Describe the morphology of the erythrocytes.
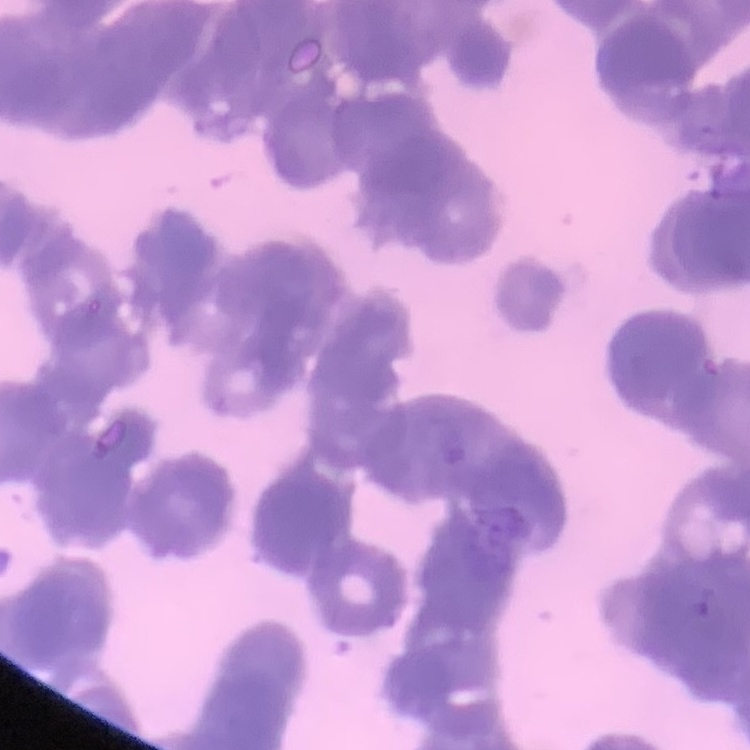

They show rouleaux formation.

Thin peripheral smear. Field's or Giemsa stain. Square crop of a larger photomicrograph.